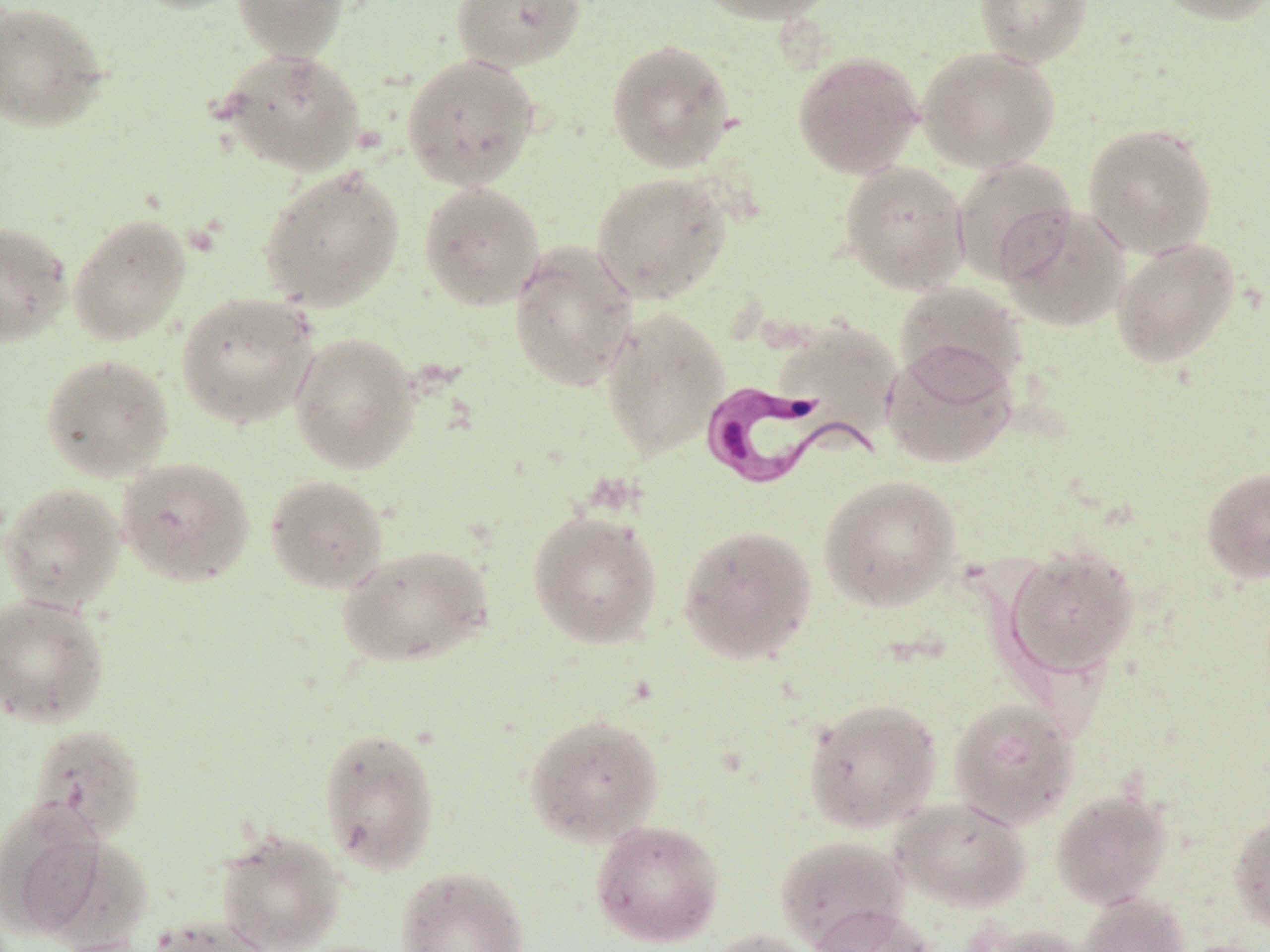
Approximate bounding boxes as (x1, y1, x2, y2) in pixels. Uninfected red blood cell locations: (127, 0, 256, 15), (231, 0, 349, 62), (450, 0, 587, 72), (689, 0, 842, 25), (974, 0, 1092, 66), (1150, 0, 1270, 25), (0, 1, 112, 133), (605, 38, 737, 174), (916, 46, 1060, 173), (218, 47, 366, 175), (792, 50, 923, 178), (401, 53, 541, 191), (1083, 123, 1218, 258), (951, 156, 1077, 284), (839, 160, 970, 294), (259, 167, 404, 311), (591, 171, 732, 304), (419, 180, 544, 310), (998, 206, 1131, 333), (68, 214, 191, 346), (0, 221, 73, 346), (1111, 237, 1240, 369), (508, 241, 639, 391), (895, 281, 1028, 394), (175, 292, 319, 428), (600, 306, 730, 460), (772, 319, 903, 442), (288, 331, 420, 474), (881, 342, 1017, 470), (40, 353, 174, 481), (116, 456, 255, 587), (1201, 466, 1270, 585), (265, 473, 388, 594), (817, 473, 963, 612), (0, 482, 125, 612), (527, 509, 664, 650), (677, 523, 818, 665), (337, 543, 494, 667), (1004, 544, 1140, 677), (0, 594, 110, 729), (802, 697, 942, 832), (949, 697, 1080, 828), (522, 712, 665, 847), (25, 723, 147, 845), (317, 725, 441, 875), (1050, 789, 1173, 908), (889, 796, 1032, 912), (0, 799, 117, 942), (1229, 811, 1270, 933), (590, 820, 724, 947), (215, 829, 346, 952), (774, 834, 909, 949), (36, 836, 153, 952), (395, 865, 530, 952), (1078, 892, 1190, 952), (808, 904, 937, 952), (146, 915, 276, 952), (966, 923, 1089, 952), (706, 928, 824, 952). Trypanosoma brucei locations: (698, 381, 882, 491). Slide-level diagnosis: Trypanosoma brucei. One field of a larger specimen. Thin blood smear. Image is 1270×952 pixels. 1000x magnification. May-Grünwald-Giemsa stain. Optical microscopy.